Locate every malaria parasite.
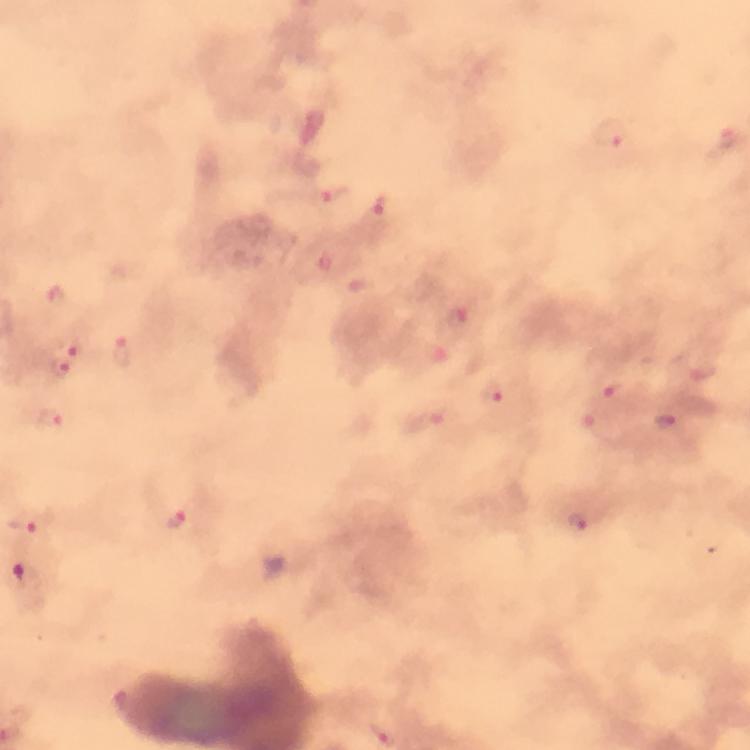
Approximate centers as [x, y] in pixels.
Malaria parasites: [609, 134], [328, 199], [380, 210], [55, 298], [69, 347], [121, 351], [61, 369], [702, 372], [613, 389], [493, 393], [50, 419], [660, 420], [598, 425], [177, 520], [580, 522], [25, 525].

Summary:
  - Magnification: 100x
  - Immersion oil: used
  - Capture: smartphone photograph through a microscope
  - Preparation: thick smear
  - Context: from a malaria diagnostic workup
  - Stain: Giemsa
  - Image size: 750×750 pixels
  - Cropped from: a single field of view